Assess this cell for malaria.
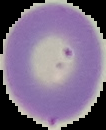

Uninfected.

preparation = thin blood film
image size = 106×130 pixels
image type = segmented cell region with the area outside set to black